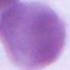
magnification: 1000x
identification: erythrocyte
modality: photomicrograph